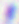
{
  "modality": "photomicrograph",
  "identification": "Toxoplasma gondii",
  "magnification": "400x"
}